State the blood parasite species.
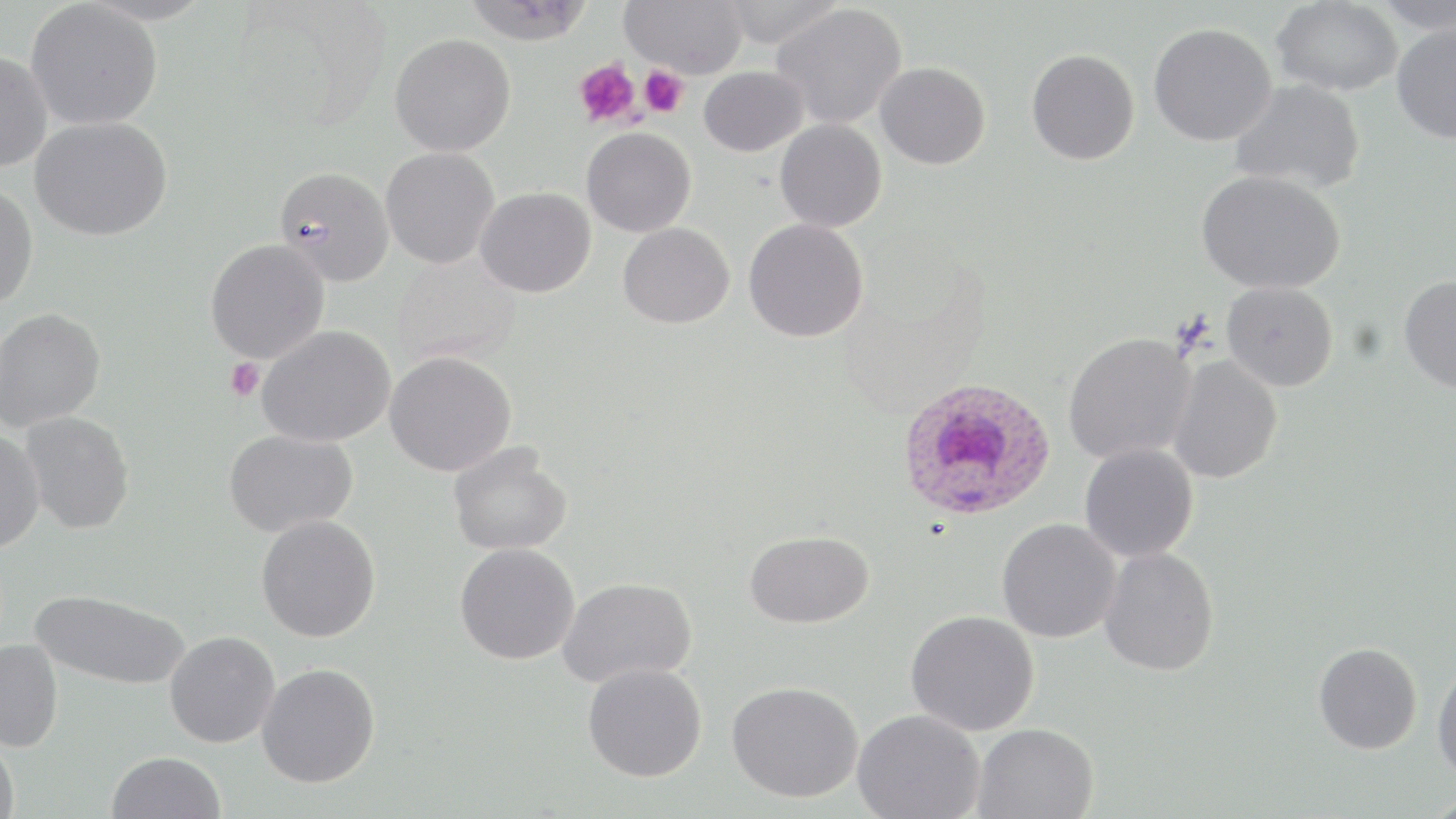

Plasmodium ovale.

Approximate bounding boxes as (x1,y1)-(x2,y2) corner pairs in pixels. Plasmodium ovale-infected red blood cell locations: (896,375)-(1056,522). Platelet locations: (573,58)-(641,128), (639,66)-(688,117), (224,358)-(265,402). Uninfected red blood cell locations: (462,0)-(595,45), (620,0)-(748,78), (717,0)-(845,49), (1374,0)-(1456,35), (26,1)-(163,130), (1271,1)-(1404,96), (772,3)-(907,130), (1392,22)-(1456,143), (1148,23)-(1277,147), (390,33)-(516,156), (1026,49)-(1140,165), (0,52)-(53,173), (875,62)-(990,170), (699,66)-(808,157), (1229,79)-(1366,194), (31,117)-(173,241), (775,119)-(887,232), (582,127)-(696,237), (381,147)-(500,268), (274,166)-(394,286), (1196,170)-(1345,295), (0,182)-(39,310), (475,187)-(596,298), (744,218)-(869,342), (618,222)-(735,328), (205,239)-(330,364), (1398,274)-(1456,393), (1221,281)-(1338,391), (0,307)-(106,432), (257,325)-(396,447), (1062,331)-(1197,464), (385,351)-(516,476), (1168,355)-(1283,485), (20,411)-(135,534), (0,429)-(45,553), (223,429)-(358,537), (448,441)-(573,556), (1079,442)-(1199,562), (256,514)-(381,642), (996,518)-(1122,643), (744,529)-(874,629), (454,543)-(580,665), (1099,547)-(1219,676), (557,577)-(697,689), (29,588)-(190,690), (905,610)-(1040,736), (164,631)-(280,748), (0,639)-(64,753), (1314,642)-(1422,754), (582,662)-(707,782), (1432,662)-(1456,781), (256,663)-(381,788), (726,680)-(864,803), (853,709)-(985,819), (973,723)-(1098,819), (0,737)-(20,819), (106,751)-(225,819). Optical microscopy. May-Grünwald-Giemsa-stained preparation. Image is 1456×819 pixels. Thin blood smear. Captured at 1000x magnification. One field of a larger specimen.